Locate every Plasmodium parasite.
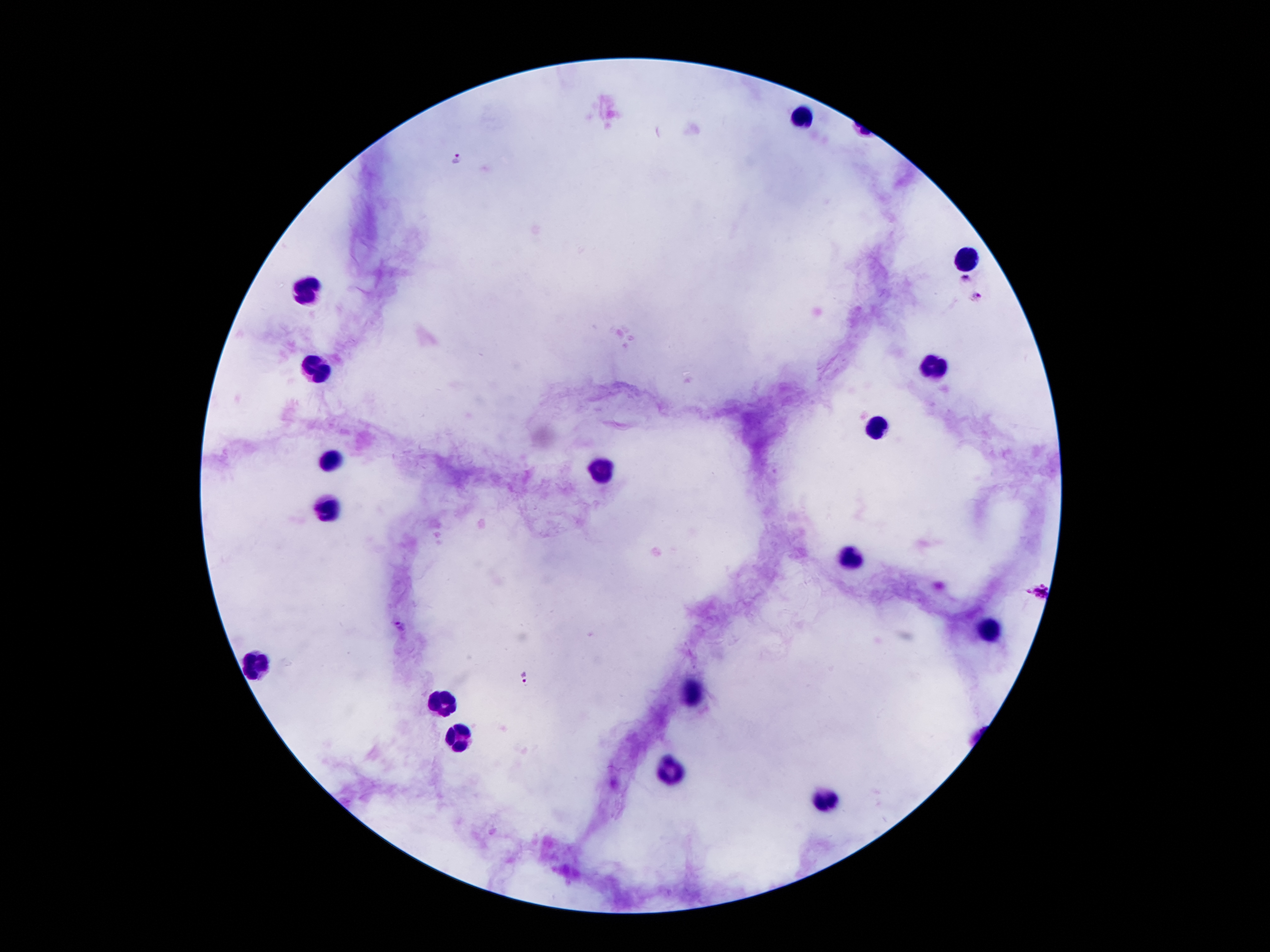
Approximate centers as [x, y] in pixels.
Plasmodium parasites: [458, 159], [965, 277], [976, 298], [1034, 590], [399, 625], [526, 674].

leukocyte locations = [805, 115], [967, 258], [306, 288], [320, 367], [932, 367], [876, 424], [333, 462], [604, 472], [329, 513], [855, 556], [992, 630], [259, 664], [697, 692], [445, 703], [458, 735], [669, 771], [828, 799]
image size = 1270×952 pixels
stain = Giemsa
preparation = thick blood film
capture = smartphone through the microscope eyepiece
patient malaria status = infected with Plasmodium falciparum
field of view = one from this slide
magnification = 100x